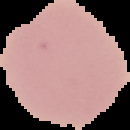

Summary:
  - Preparation: thin blood film
  - Image type: segmented cell region with the area outside set to black
  - Malaria status: uninfected
  - Image size: 130×130 pixels